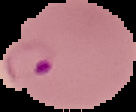
{
  "image_size": "136×112 pixels",
  "malaria_status": "parasitized",
  "image_type": "segmented cell region with the area outside set to black",
  "preparation": "thin blood smear"
}